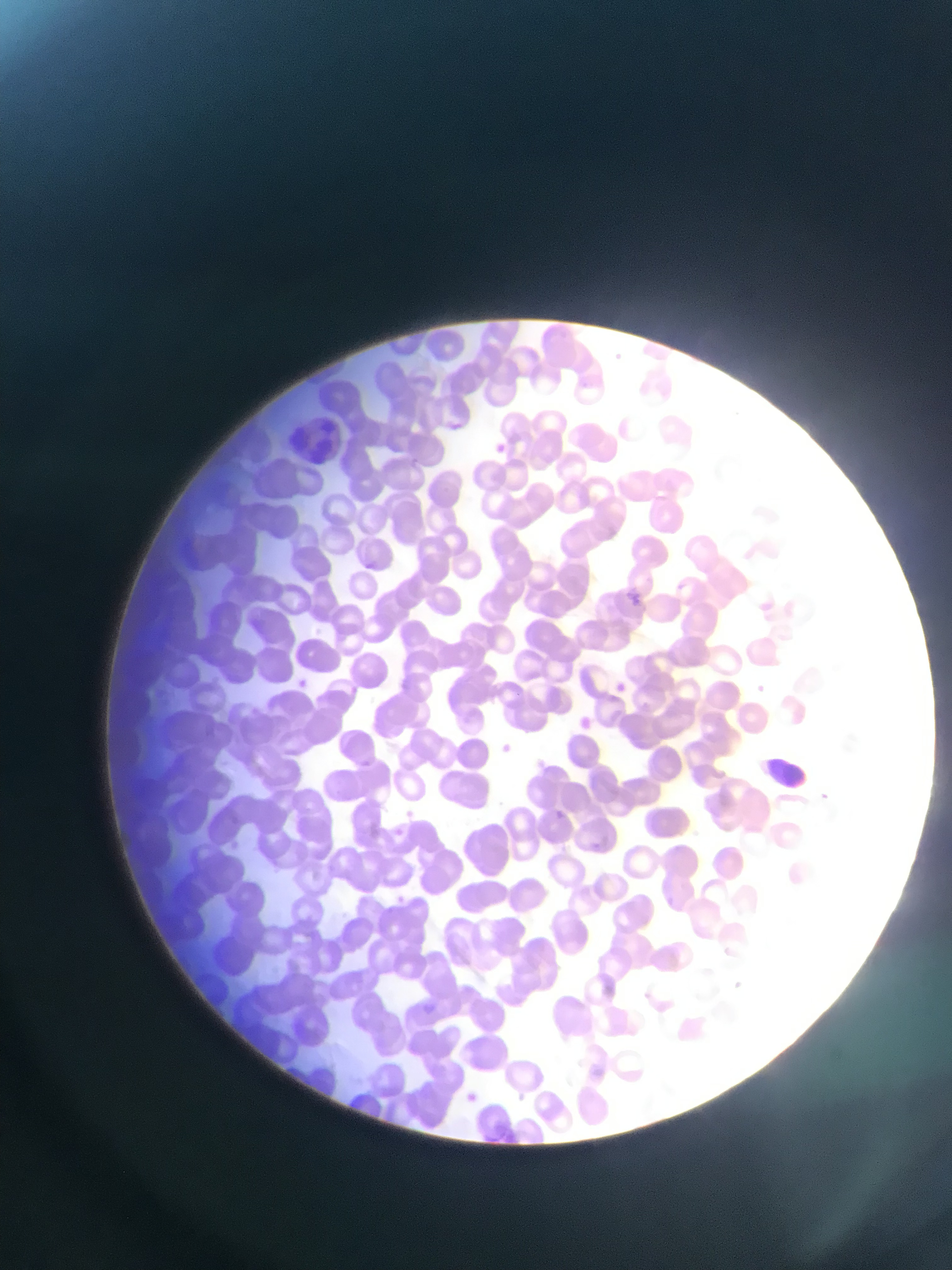

preparation: thin blood smear
image_size: 952×1270 pixels
capture: mobile-phone photograph through a microscope
plasmodium_parasite_locations: 'approximate bounding boxes as [left, top, right, bottom] in pixels: [441, 421, 461, 431], [490, 437, 508, 452], [360, 559, 373, 567], [626, 588, 647, 615], [295, 673, 325, 708], [613, 676, 632, 689], [579, 712, 600, 735], [355, 758, 387, 783], [547, 807, 563, 817], [422, 1002, 437, 1019], [463, 1086, 467, 1103]'
field_of_view: single
country: Ghana
leukocyte_locations: 'approximate bounding boxes as [left, top, right, bottom] in pixels: [291, 412, 360, 460], [754, 746, 830, 802]'